Comment on the morphology of the erythrocytes.
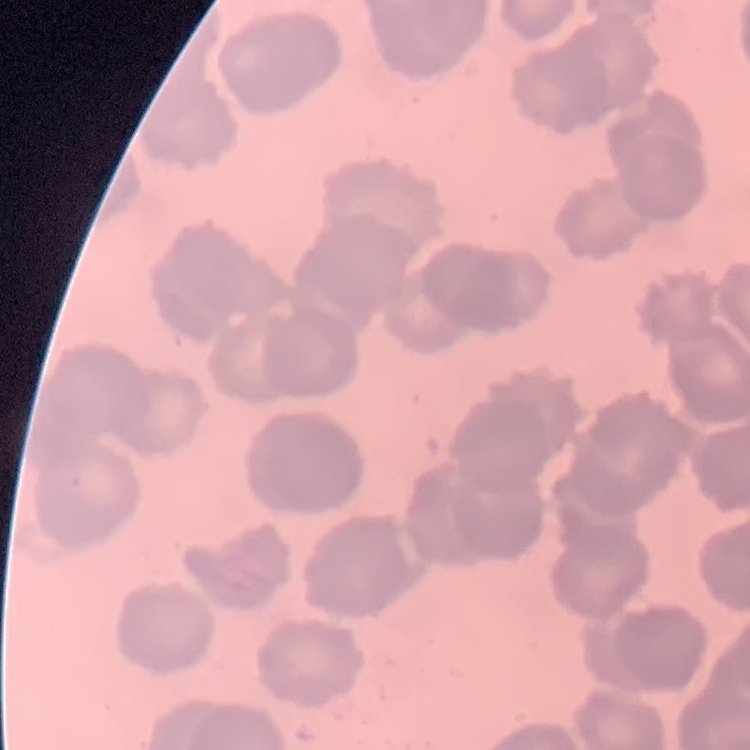

They show rouleaux formation.

Thin blood smear. Field's or Giemsa stain. Square crop of a larger photomicrograph.